Locate every malaria parasite and identify its life-cycle stage.
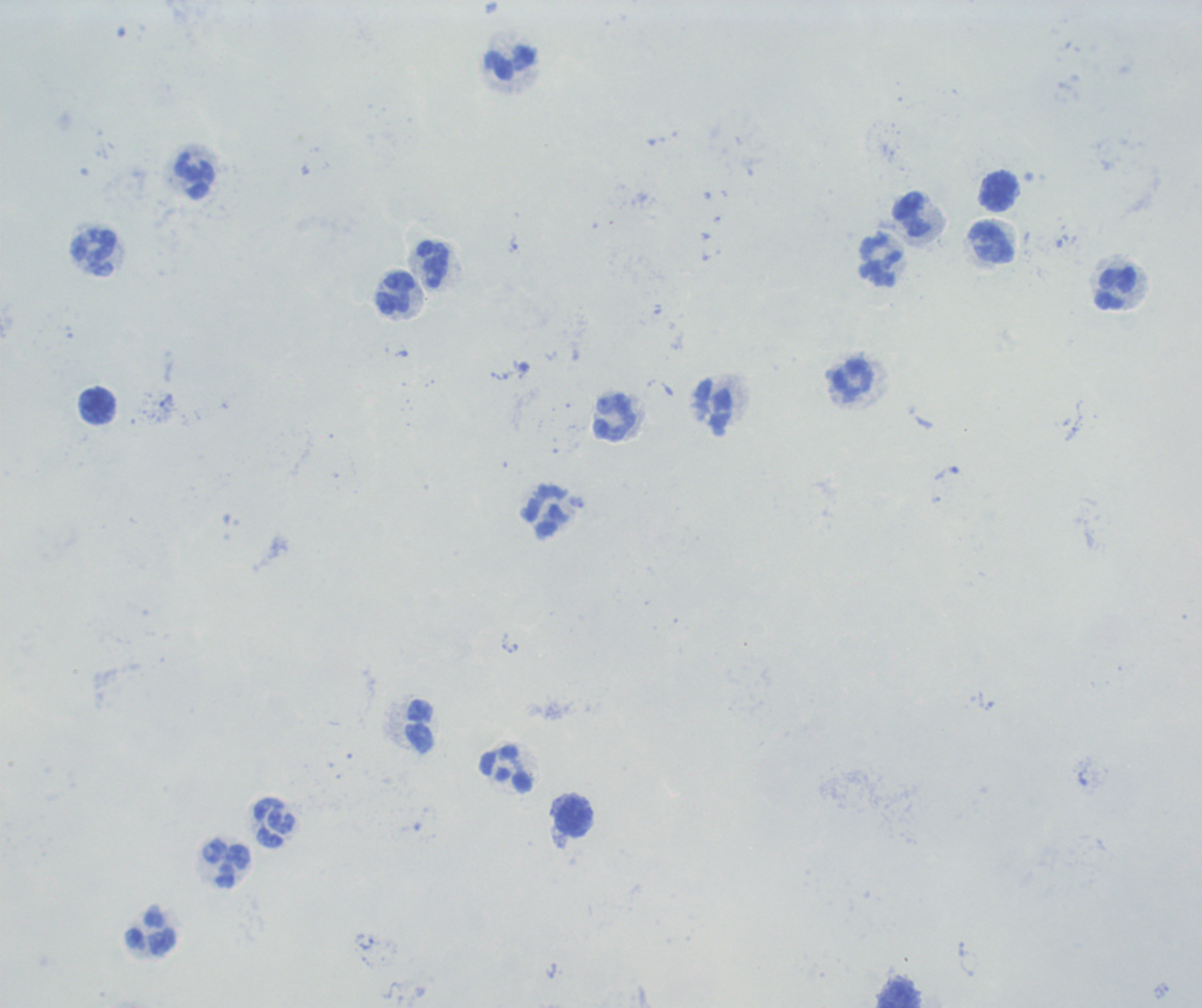

No malaria parasites detected.

{
  "stain": "Romanowsky",
  "magnification": "100x",
  "context": "previously used in a real diagnosis",
  "preparation": "thick blood film",
  "image_size": "1202×1008 pixels",
  "background_quality": "unsatisfactory",
  "leukocyte_locations": "approximate centers as (x, y) in pixels: (511, 64), (194, 175), (1000, 192), (912, 214), (993, 243), (94, 253), (881, 260), (433, 264), (1116, 289), (395, 294), (853, 380), (97, 405), (713, 408), (615, 417), (545, 511), (420, 727), (506, 770), (574, 815), (274, 823), (227, 864), (150, 935), (900, 995)",
  "field_of_view": "one from this slide"
}